State which parasite is depicted.
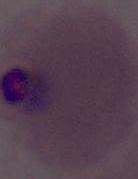

Plasmodium.

400x or 1000x magnification. Photomicrograph.